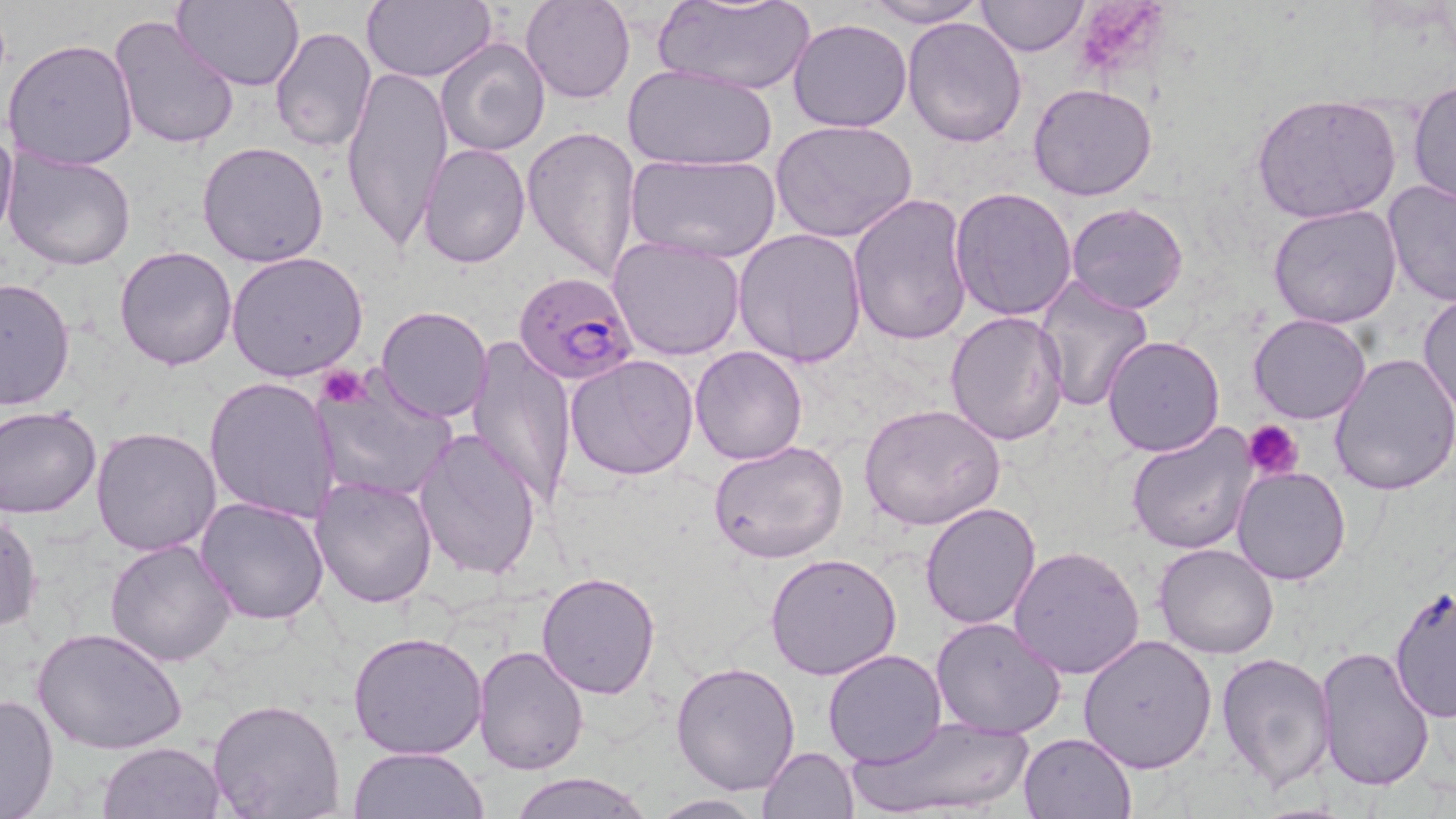
slide_level_diagnosis: Plasmodium falciparum
modality: optical microscopy
preparation: thin blood smear
image_size: 1456×819 pixels
field_of_view: single
magnification: 1000x
stain: May-Grünwald-Giemsa
plasmodium_falciparum_infected_red_blood_cell_locations: 'approximate bounding boxes as [x1, y1, x2, y2] in pixels: [513, 271, 640, 386]'
platelet_locations: 'approximate bounding boxes as [x1, y1, x2, y2] in pixels: [316, 365, 368, 409], [1243, 420, 1302, 478]'
uninfected_red_blood_cell_locations: 'approximate bounding boxes as [x1, y1, x2, y2] in pixels: [173, 0, 304, 91], [361, 0, 495, 83], [520, 0, 634, 104], [859, 0, 987, 27], [974, 0, 1088, 57], [653, 1, 816, 95], [109, 15, 240, 155], [788, 18, 911, 132], [902, 18, 1027, 148], [268, 26, 376, 156], [436, 36, 550, 157], [4, 37, 139, 172], [341, 64, 452, 258], [625, 64, 777, 168], [1409, 81, 1456, 210], [1028, 83, 1160, 202], [1252, 93, 1401, 225], [0, 115, 18, 245], [771, 118, 919, 244], [521, 124, 641, 281], [198, 140, 330, 267], [420, 141, 531, 269], [4, 151, 137, 272], [626, 153, 782, 263], [1381, 179, 1456, 304], [949, 188, 1078, 323], [846, 193, 976, 348], [1063, 203, 1189, 315], [1268, 205, 1402, 329], [733, 227, 868, 368], [608, 235, 746, 361], [114, 246, 237, 371], [226, 250, 370, 380], [0, 275, 74, 411], [1033, 275, 1157, 412], [1418, 292, 1456, 417], [375, 306, 494, 424], [944, 311, 1069, 448], [1247, 314, 1372, 425], [1101, 335, 1225, 457], [464, 337, 576, 508], [689, 346, 810, 465], [1329, 350, 1456, 497], [564, 353, 699, 480], [205, 376, 340, 524], [316, 376, 455, 505], [860, 404, 1005, 531], [0, 406, 102, 519], [1125, 422, 1261, 557], [91, 426, 222, 557], [415, 429, 543, 583], [709, 441, 848, 564], [1231, 465, 1354, 585], [310, 477, 438, 609], [192, 497, 331, 627], [918, 502, 1041, 630], [1, 506, 41, 634], [104, 537, 239, 667], [1154, 542, 1278, 659], [1009, 546, 1145, 680], [765, 553, 902, 681], [535, 571, 663, 700], [1388, 585, 1455, 723], [930, 616, 1068, 739], [34, 627, 187, 756], [347, 631, 488, 759], [1077, 634, 1217, 774], [472, 644, 591, 775], [1315, 644, 1437, 791], [823, 649, 946, 768], [1216, 650, 1337, 790], [672, 662, 802, 796], [0, 691, 58, 819], [207, 699, 346, 819], [849, 713, 1036, 819], [1018, 731, 1136, 818], [98, 742, 224, 819], [759, 745, 859, 818], [351, 747, 487, 819], [510, 771, 652, 818], [648, 793, 767, 818]'